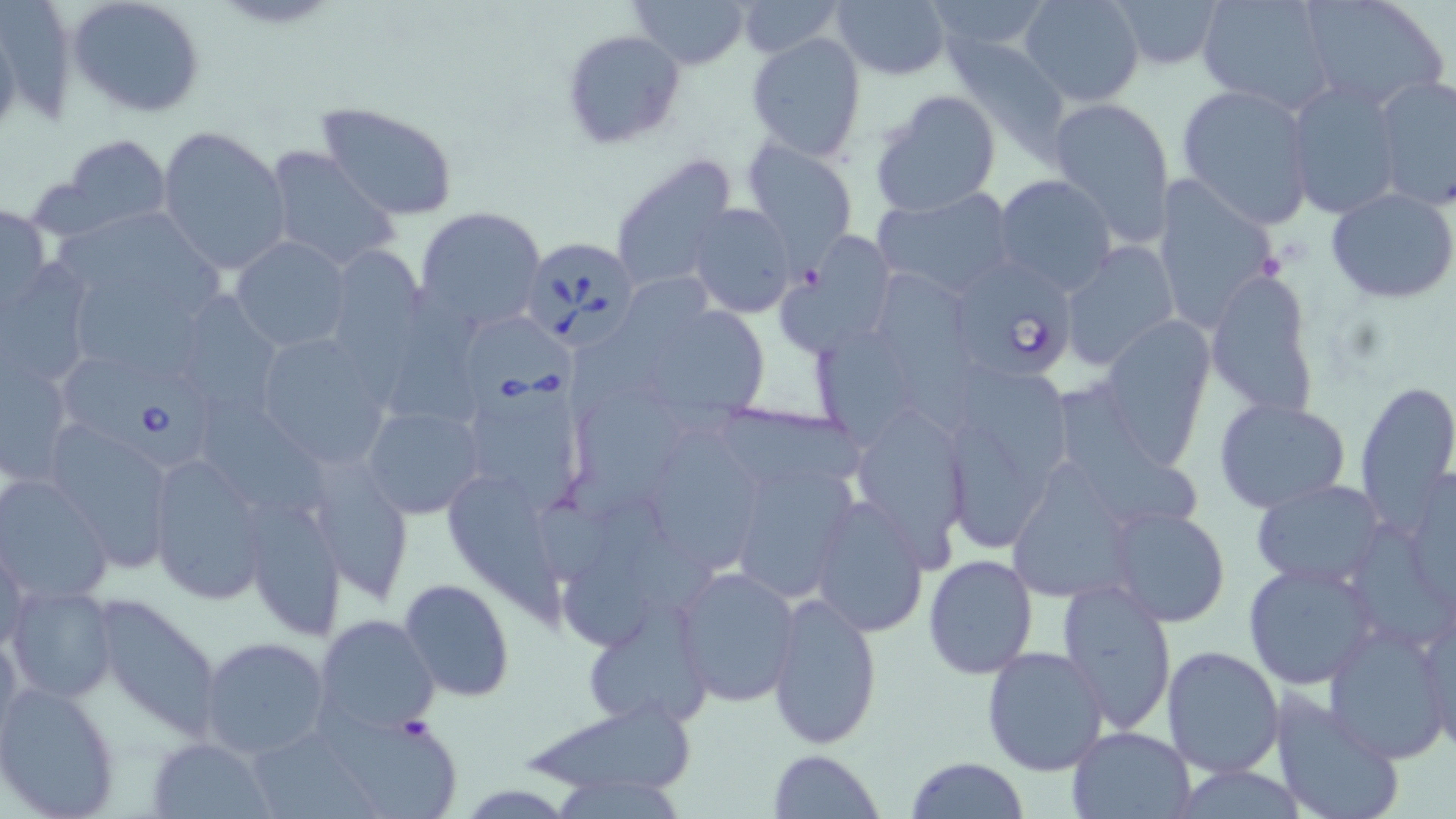 Approximate bounding boxes as (x1, y1, x2, y2) in pixels. Uninfected red blood cell locations: (67, 0, 205, 118), (627, 0, 749, 70), (830, 0, 950, 80), (926, 0, 1059, 63), (1019, 0, 1145, 106), (1104, 0, 1226, 70), (1194, 0, 1337, 115), (1298, 0, 1449, 111), (734, 1, 846, 59), (560, 29, 685, 150), (746, 33, 867, 161), (947, 39, 1071, 163), (5, 40, 77, 125), (1373, 76, 1456, 208), (1284, 80, 1404, 220), (1175, 83, 1317, 230), (871, 89, 1003, 216), (1048, 97, 1176, 247), (315, 103, 459, 221), (157, 126, 291, 273), (60, 134, 172, 233), (745, 141, 858, 260), (263, 145, 399, 274), (610, 154, 739, 291), (1151, 174, 1282, 328), (993, 175, 1116, 295), (1326, 188, 1456, 302), (870, 189, 1018, 300), (0, 202, 51, 316), (686, 202, 796, 318), (53, 203, 234, 314), (415, 206, 547, 334), (784, 234, 896, 355), (232, 237, 351, 352), (1060, 241, 1179, 371), (328, 246, 427, 366), (1, 261, 96, 389), (878, 269, 981, 436), (1204, 269, 1320, 421), (75, 273, 206, 383), (570, 277, 709, 434), (389, 281, 491, 425), (167, 291, 286, 422), (631, 300, 772, 426), (1097, 314, 1214, 466), (802, 319, 932, 450), (253, 330, 397, 472), (0, 356, 76, 488), (962, 366, 1074, 503), (456, 374, 589, 516), (569, 379, 695, 520), (1353, 379, 1456, 525), (1058, 383, 1205, 527), (1213, 397, 1351, 512), (203, 398, 333, 515), (362, 402, 484, 519), (851, 402, 974, 559), (720, 406, 863, 490), (46, 422, 177, 569), (944, 423, 1034, 555), (646, 433, 766, 575), (148, 453, 271, 605), (724, 457, 853, 599), (306, 459, 414, 602), (1006, 460, 1141, 602), (0, 474, 115, 605), (440, 476, 567, 633), (1249, 478, 1387, 590), (245, 495, 345, 639), (807, 495, 931, 638), (561, 499, 679, 649), (1105, 505, 1231, 628), (1348, 521, 1455, 651), (1, 534, 28, 664), (921, 554, 1038, 679), (1243, 561, 1380, 689), (673, 565, 801, 707), (1055, 576, 1177, 736), (399, 578, 515, 703), (6, 583, 118, 703), (766, 591, 882, 748), (91, 592, 225, 739), (1416, 600, 1456, 757), (581, 602, 713, 731), (313, 614, 440, 738), (1325, 624, 1452, 760), (0, 627, 26, 761), (198, 636, 331, 758), (1161, 644, 1287, 778), (981, 645, 1109, 774), (0, 682, 122, 819), (1268, 691, 1404, 819), (515, 699, 699, 801), (320, 709, 464, 819), (1068, 725, 1198, 818), (251, 732, 383, 819), (146, 738, 275, 819), (767, 748, 885, 818), (905, 756, 1030, 819), (1169, 764, 1311, 819), (546, 775, 686, 816). Babesia divergens-infected red blood cell locations: (522, 235, 639, 346), (958, 258, 1076, 383), (465, 312, 581, 424), (56, 361, 221, 473). Slide-level diagnosis: Babesia divergens. 1000x magnification. May-Grünwald-Giemsa-stained preparation. Image is 1456×819 pixels. Thin blood smear. One field of a larger specimen. Optical microscopy.